State the blood parasite species.
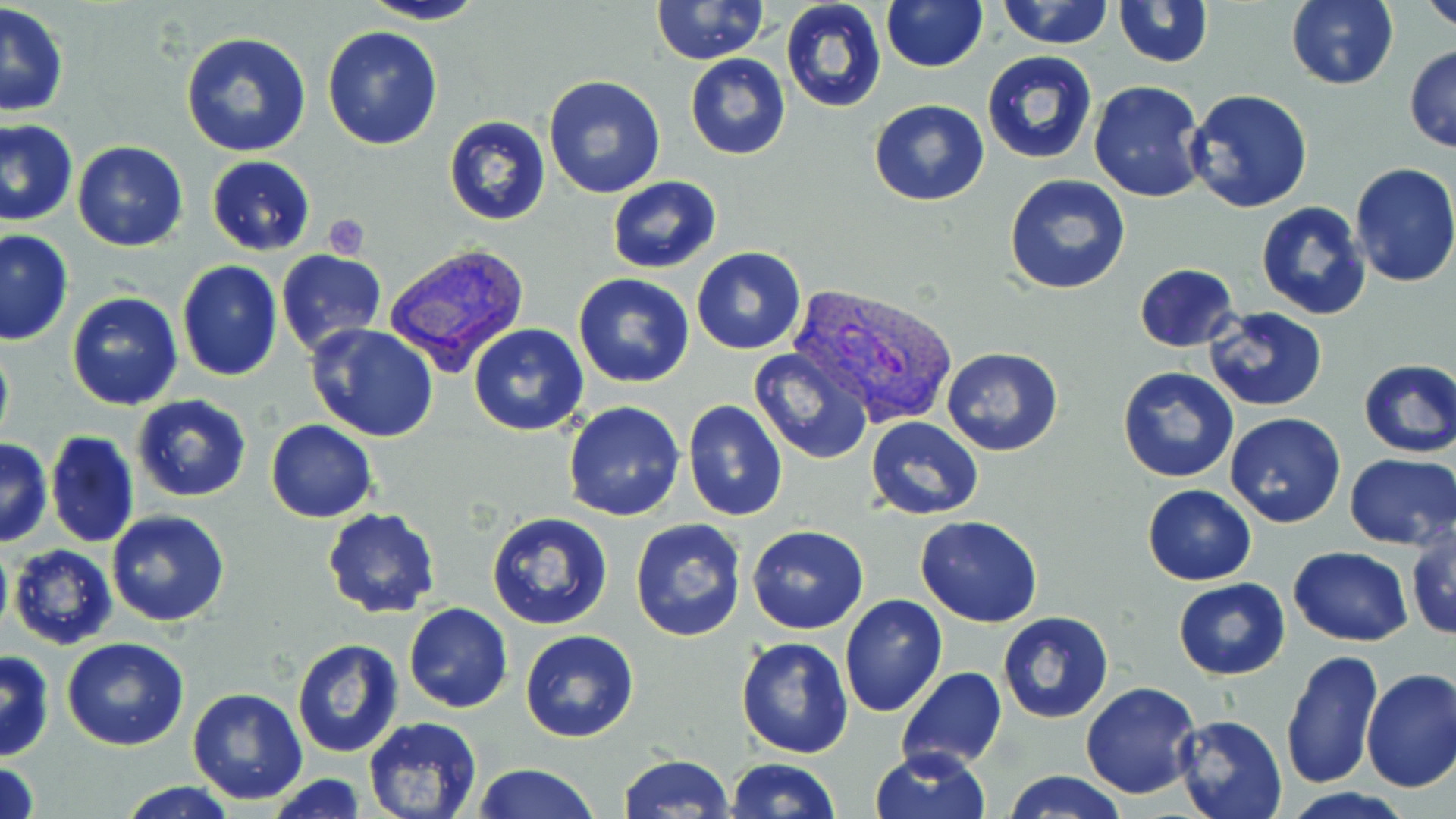

Plasmodium vivax.

field of view = one of a larger specimen
magnification = 1000x
modality = light microscopy
preparation = thin blood smear
image size = 1456×819 pixels
platelet locations = approximate bounding boxes as (x1,y1)-(x2,y2) corner pairs in pixels: (322,214)-(370,261)
stain = May-Grünwald-Giemsa
uninfected red blood cell locations = approximate bounding boxes as (x1,y1)-(x2,y2) corner pairs in pixels: (361,0)-(491,26), (651,0)-(769,65), (881,0)-(987,72), (996,0)-(1113,48), (1114,0)-(1214,69), (1285,0)-(1400,91), (1421,0)-(1456,32), (780,1)-(886,116), (0,4)-(70,118), (322,25)-(445,149), (180,32)-(312,159), (1404,46)-(1455,154), (982,50)-(1100,166), (685,53)-(791,160), (543,75)-(667,199), (1088,80)-(1210,202), (1184,88)-(1314,213), (868,99)-(989,206), (441,116)-(551,227), (1,119)-(77,227), (72,140)-(188,251), (206,156)-(316,256), (1349,163)-(1456,287), (1003,173)-(1131,294), (607,176)-(722,273), (1257,200)-(1372,321), (0,229)-(75,345), (691,247)-(806,355), (275,249)-(387,356), (176,262)-(284,382), (1134,264)-(1241,352), (572,274)-(694,388), (64,290)-(183,411), (1203,306)-(1328,412), (468,323)-(592,437), (307,325)-(440,442), (0,337)-(14,451), (749,346)-(874,464), (941,347)-(1065,458), (1356,359)-(1456,457), (1116,366)-(1238,483), (132,395)-(253,502), (563,400)-(686,521), (683,400)-(787,520), (1224,412)-(1346,527), (865,417)-(983,520), (265,420)-(377,523), (44,430)-(139,547), (0,439)-(52,545), (1345,452)-(1456,551), (1141,484)-(1258,584), (321,508)-(441,621), (106,510)-(232,627), (486,510)-(614,630), (915,516)-(1043,626), (629,518)-(745,644), (748,525)-(869,634), (1405,525)-(1456,640), (0,537)-(12,642), (9,544)-(117,649), (1288,546)-(1413,646), (1174,579)-(1289,679), (840,593)-(948,717), (403,603)-(513,713), (997,611)-(1115,724), (519,630)-(639,742), (736,635)-(854,758), (62,638)-(189,751), (291,639)-(403,758), (1281,649)-(1384,791), (0,651)-(54,761), (1360,667)-(1456,792), (897,668)-(1007,773), (1079,682)-(1202,801), (187,688)-(309,804), (1172,713)-(1286,819), (363,716)-(486,819), (870,747)-(991,819), (618,753)-(735,818), (0,757)-(39,819), (726,757)-(841,818), (469,762)-(600,819), (1002,770)-(1128,819), (266,774)-(372,819), (114,780)-(243,818)
Plasmodium vivax-infected red blood cell locations = approximate bounding boxes as (x1,y1)-(x2,y2) corner pairs in pixels: (383,243)-(531,377), (792,281)-(956,426)